Report the malaria status of this cell.
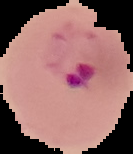
It is parasitized.

From a thin blood film. Image is 133×154 pixels. The area outside the segmented cell region is set to black.